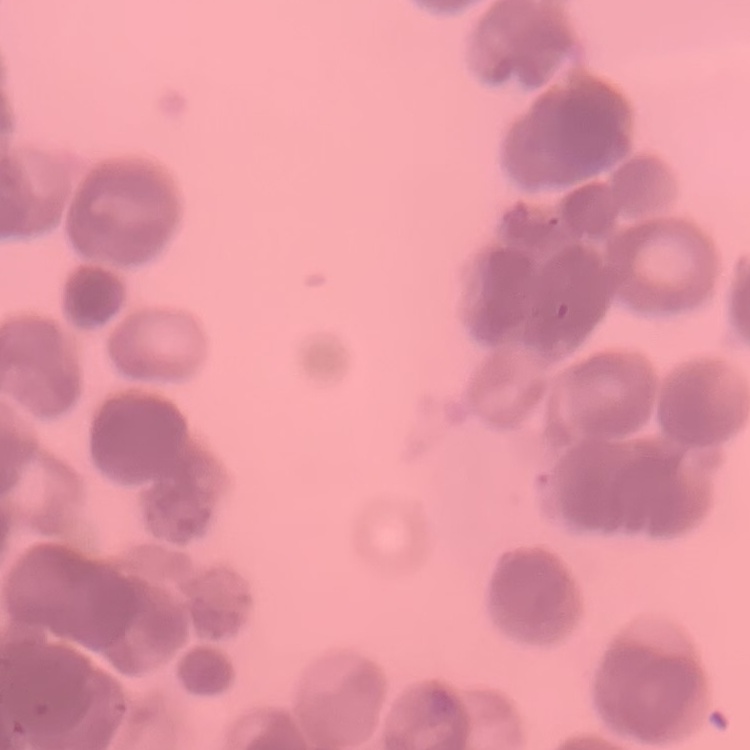

Summary:
  - Erythrocyte morphology: rouleaux formation
  - Stain: Field's or Giemsa
  - Image type: one tile cut from a larger photomicrograph
  - Preparation: thin peripheral smear